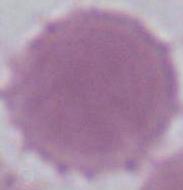
An erythrocyte is seen. Micrograph. Captured at 1000x magnification.